Classify this cell by malaria status.
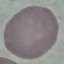
Uninfected.

image type = automatically extracted cell patch, resized to 64 × 64 pixels
capture = smartphone camera at the microscope eyepiece
preparation = thin smear
stain = Giemsa